Report the malaria status of this cell.
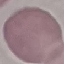
It is uninfected.

preparation: thin blood smear
image_type: automatically extracted cell patch, resized to 64 × 64 pixels
capture: smartphone camera at the microscope eyepiece
stain: Giemsa